Mark where leukocytes are.
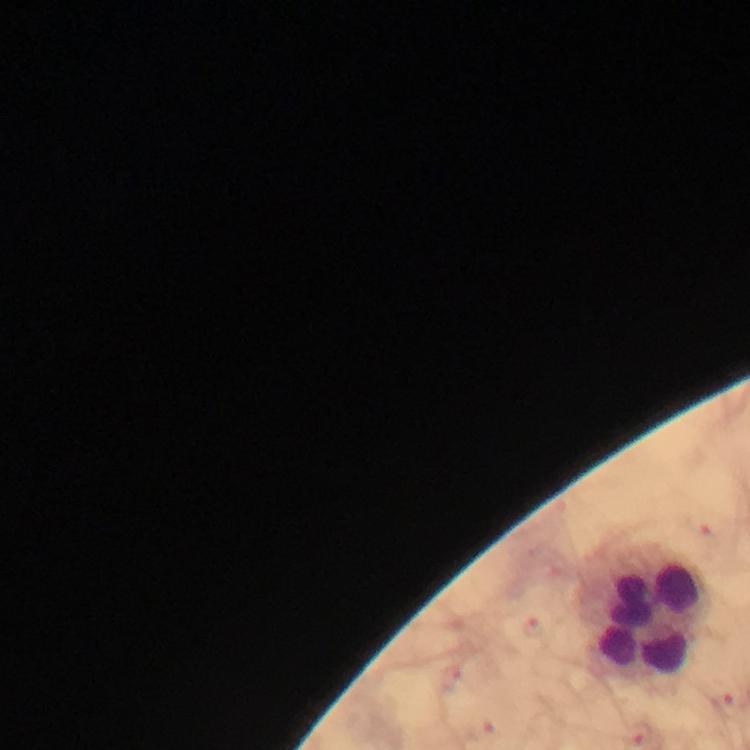

Approximate centers as {x, y} in pixels.
Leukocytes: {644, 616}.

Summary:
  - Magnification: 100x
  - Context: from a malaria diagnostic workup
  - Capture: smartphone mounted on the microscope
  - Immersion oil: applied
  - Image size: 750×750 pixels
  - Cropped from: one field of view
  - Plasmodium parasites: none seen
  - Stain: Giemsa
  - Preparation: thick smear